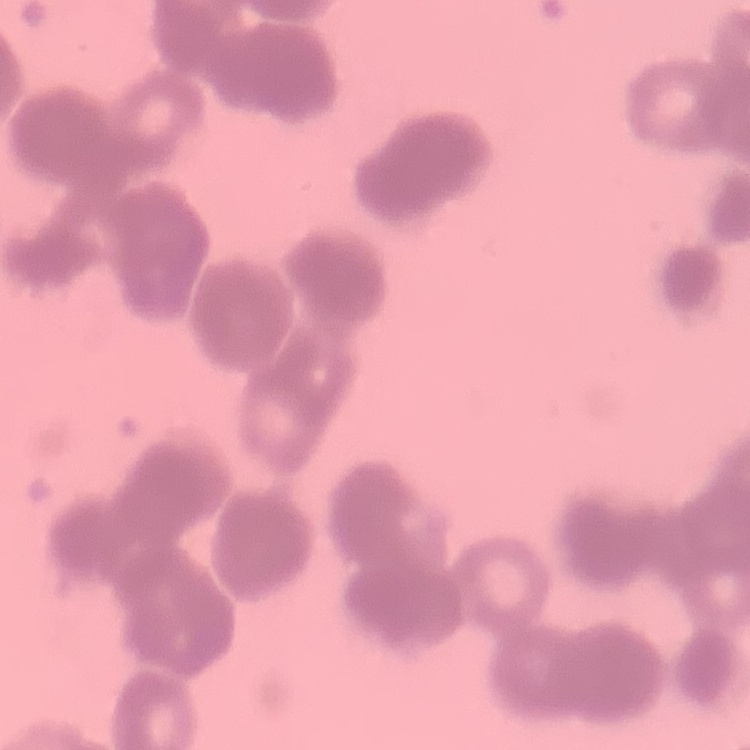

The erythrocytes exhibit rouleaux formation. Thin blood smear. Stained with either Field's or Giemsa. Square crop of a larger photomicrograph.